Report the malaria status of this cell.
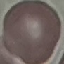

Uninfected.

Giemsa stain. Acquired by smartphone through the microscope eyepiece. Cell patch, automatically extracted from a larger field of view and resized to 64 × 64 pixels. Thin smear of blood.